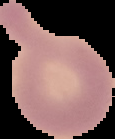
Segmented cell region on a black background. From a thin blood smear. Image is 115×139 pixels. Malaria status: uninfected.